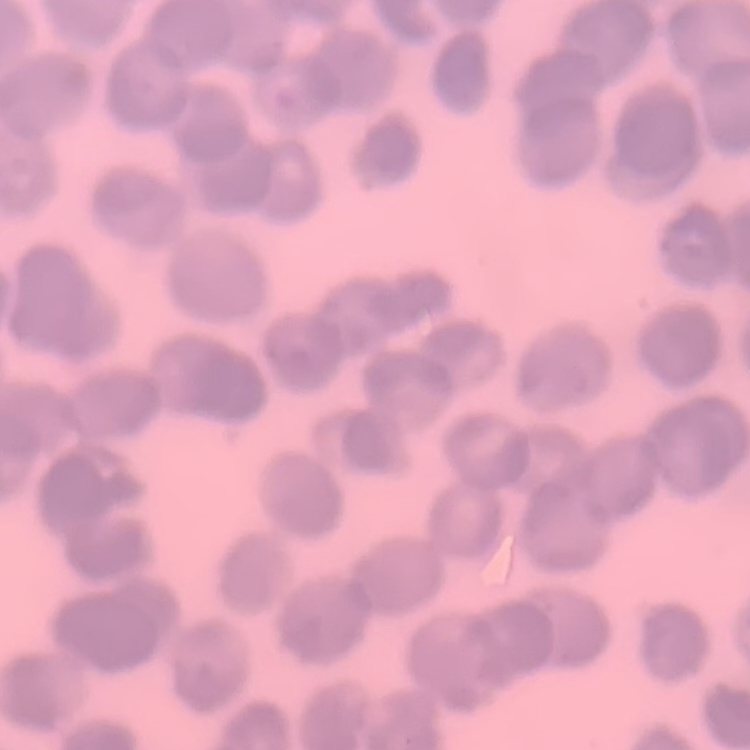

red blood cell morphology = rouleaux formation
preparation = thin blood smear
image type = square crop of a larger photomicrograph
stain = Field's or Giemsa